Describe the morphology of the erythrocytes.
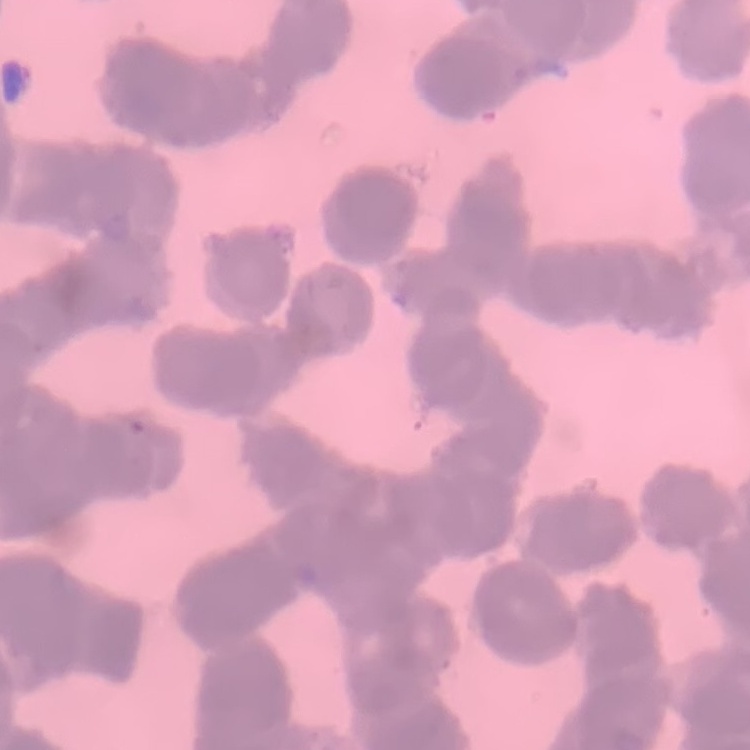
They show rouleaux formation.

image type = one tile cut from a larger photomicrograph
preparation = thin blood smear
stain = Field's or Giemsa